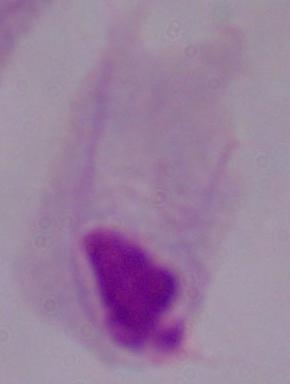
Summary:
  - Identification: trichomonad
  - Modality: photomicrograph
  - Magnification: 1000x